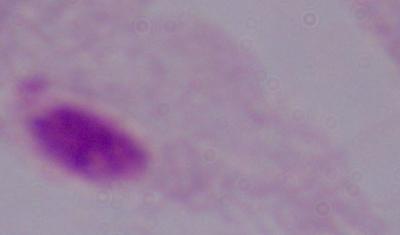

Photomicrograph. Captured at 1000x magnification. A trichomonad is shown.